State which cell type is depicted.
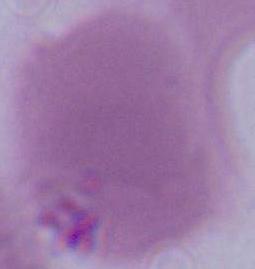
An erythrocyte.

Photomicrograph. Captured at 1000x magnification.